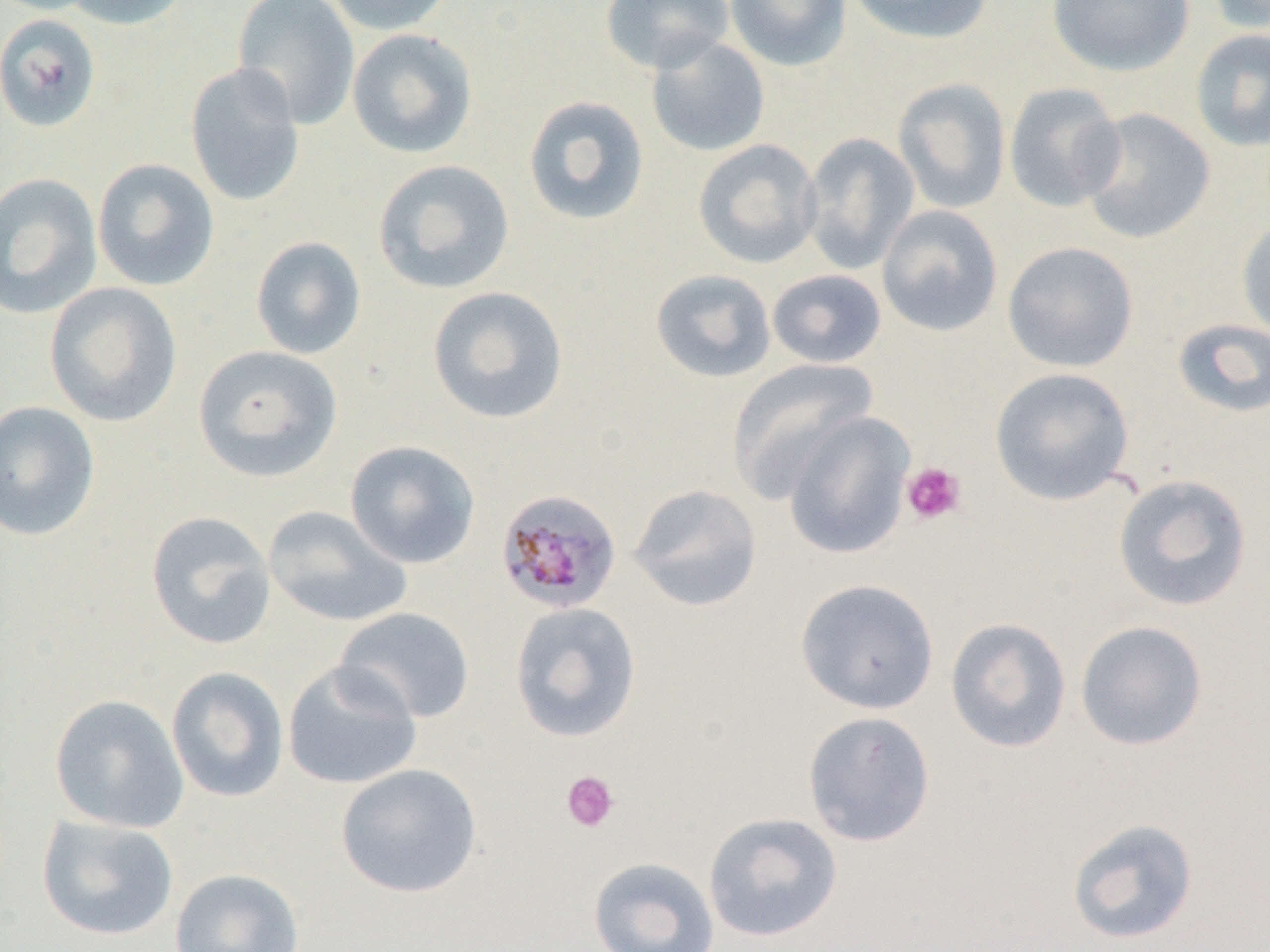
Approximate bounding boxes as [x1, y1, x2, y2] in pixels. Platelet locations: [901, 461, 967, 525], [561, 770, 620, 833]. Plasmodium malariae-infected red blood cell locations: [495, 488, 623, 615]. Uninfected red blood cell locations: [0, 0, 102, 16], [60, 0, 192, 30], [232, 0, 361, 130], [322, 0, 456, 35], [600, 0, 736, 74], [724, 0, 852, 72], [846, 0, 994, 45], [1046, 0, 1196, 77], [1203, 0, 1270, 34], [0, 14, 101, 133], [346, 27, 478, 159], [1190, 28, 1270, 152], [646, 36, 770, 157], [184, 62, 306, 208], [892, 78, 1012, 215], [1003, 83, 1127, 212], [522, 95, 650, 227], [1079, 108, 1215, 244], [800, 132, 920, 274], [693, 139, 823, 269], [92, 158, 220, 291], [372, 159, 516, 295], [0, 172, 102, 319], [876, 204, 1003, 337], [1236, 216, 1270, 343], [250, 236, 367, 360], [1002, 241, 1139, 372], [649, 269, 776, 383], [767, 269, 887, 369], [44, 282, 183, 427], [427, 286, 569, 424], [1170, 318, 1270, 418], [193, 345, 343, 482], [726, 357, 880, 502], [989, 367, 1135, 505], [0, 400, 101, 541], [781, 411, 915, 559], [345, 440, 481, 569], [1112, 473, 1252, 612], [628, 483, 763, 612], [263, 505, 412, 628], [145, 511, 277, 650], [794, 578, 939, 715], [509, 601, 641, 742], [333, 607, 476, 724], [945, 617, 1072, 753], [1074, 620, 1209, 752], [281, 659, 422, 790], [166, 666, 289, 803], [49, 694, 189, 833], [802, 710, 937, 848], [336, 763, 482, 898], [703, 811, 843, 943], [36, 814, 179, 941], [1067, 817, 1200, 944], [588, 856, 720, 952], [169, 867, 305, 952]. Slide-level diagnosis: Plasmodium malariae. Light microscopy. Image is 1270×952 pixels. One field of a larger specimen. Captured at 1000x magnification. Thin blood smear.